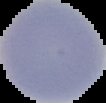

Summary:
  - Image type: segmented cell region on a black background
  - Result: no Plasmodium parasites detected
  - Image size: 106×103 pixels
  - Preparation: thin blood smear